Assess the morphology of the red blood cells.
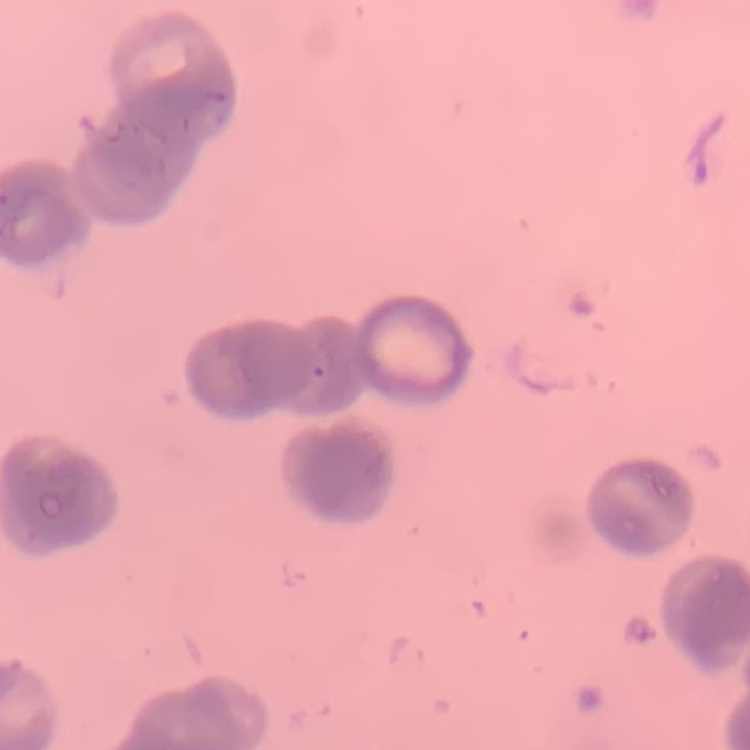

They show rouleaux formation.

Stained with either Field's or Giemsa. Square crop of a larger photomicrograph. Thin blood smear.